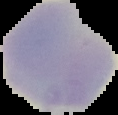 Malaria status: uninfected. Image is 118×115 pixels. From a thin blood film. The area outside the segmented cell region is set to black.